Outline each blood parasite and name the species.
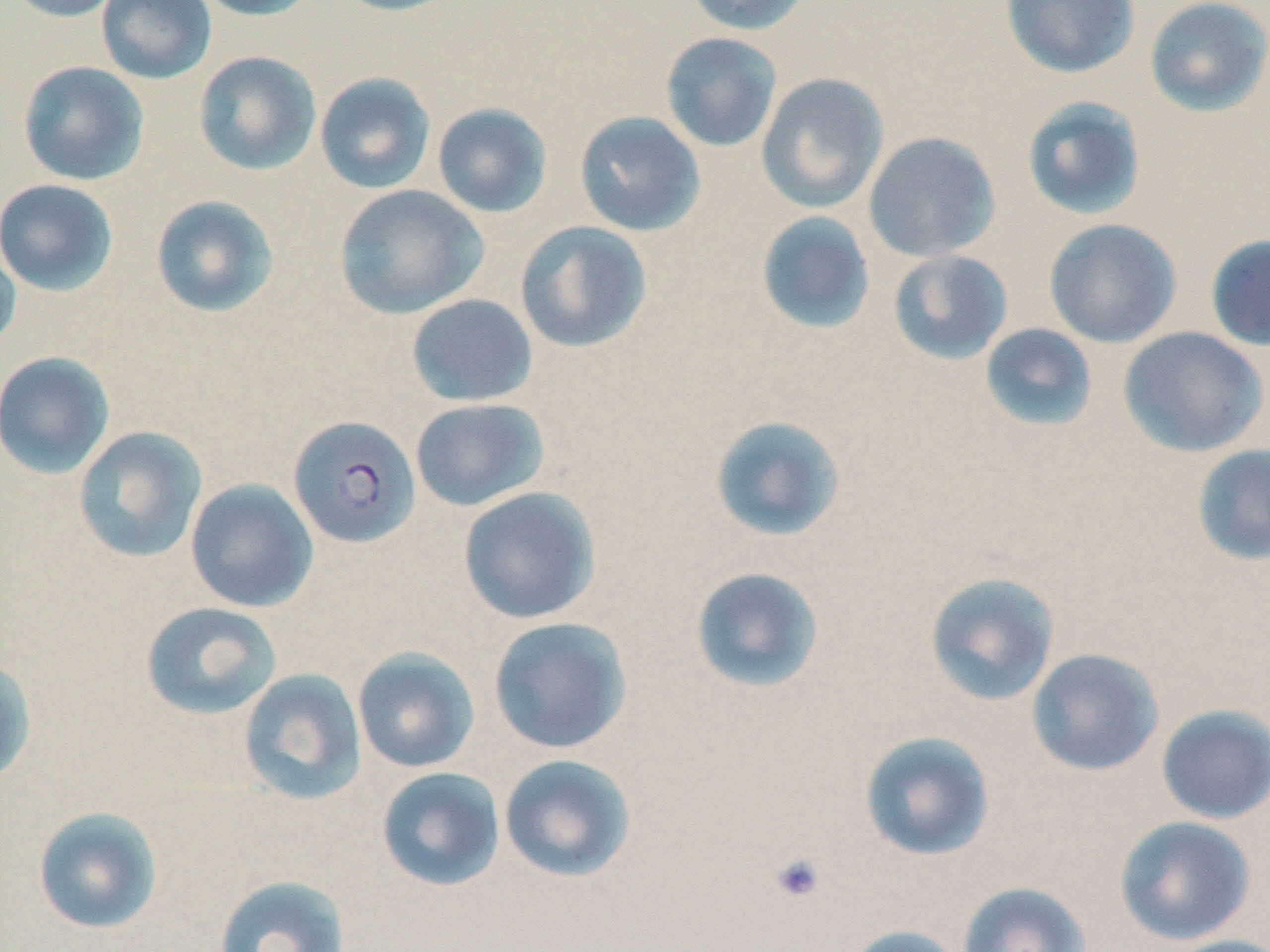

Approximate bounding boxes as (x1,y1)-(x2,y2) corner pairs in pixels.
Plasmodium falciparum-infected red blood cells: (287,414)-(421,549).
No Plasmodium ovale, Plasmodium malariae, Plasmodium vivax, Babesia divergens, or Trypanosoma brucei observed.

{
  "slide_level_diagnosis": "Plasmodium falciparum",
  "magnification": "1000x",
  "preparation": "thin blood smear",
  "uninfected_red_blood_cell_locations": "approximate bounding boxes as (x1,y1)-(x2,y2) corner pairs in pixels: (2,0)-(128,23), (96,0)-(217,84), (189,0)-(323,21), (330,0)-(459,17), (685,0)-(811,36), (1000,0)-(1140,78), (1144,0)-(1270,117), (660,32)-(783,153), (193,50)-(322,176), (17,62)-(149,186), (314,72)-(436,195), (756,72)-(889,214), (1021,96)-(1147,221), (431,102)-(553,219), (574,111)-(706,237), (863,131)-(1001,262), (0,178)-(119,296), (334,184)-(488,319), (150,195)-(280,318), (755,210)-(876,335), (1043,218)-(1181,347), (514,220)-(652,353), (1205,234)-(1270,351), (0,236)-(21,355), (888,249)-(1013,365), (405,293)-(538,407), (979,323)-(1098,432), (1117,326)-(1268,458), (0,351)-(116,479), (410,398)-(550,512), (708,414)-(847,543), (72,425)-(207,564), (1190,444)-(1270,566), (185,478)-(319,612), (457,486)-(601,624), (689,566)-(826,694), (924,570)-(1061,707), (140,601)-(282,720), (487,616)-(633,754), (352,647)-(481,773), (1026,647)-(1164,777), (0,658)-(37,785), (238,667)-(367,805), (1155,703)-(1270,824), (858,730)-(996,862), (498,753)-(637,883), (376,766)-(506,891), (32,805)-(164,935), (1113,815)-(1256,946), (213,874)-(350,952), (957,881)-(1092,952), (842,924)-(966,952), (1162,935)-(1270,952)",
  "modality": "optical microscopy",
  "field_of_view": "one of a larger specimen",
  "stain": "May-Grünwald-Giemsa",
  "platelet_locations": "approximate bounding boxes as (x1,y1)-(x2,y2) corner pairs in pixels: (769,852)-(826,903)",
  "image_size": "1270×952 pixels"
}